Give the position of each P. falciparum parasite with its life-cycle stage, each leukocyte, and any debris.
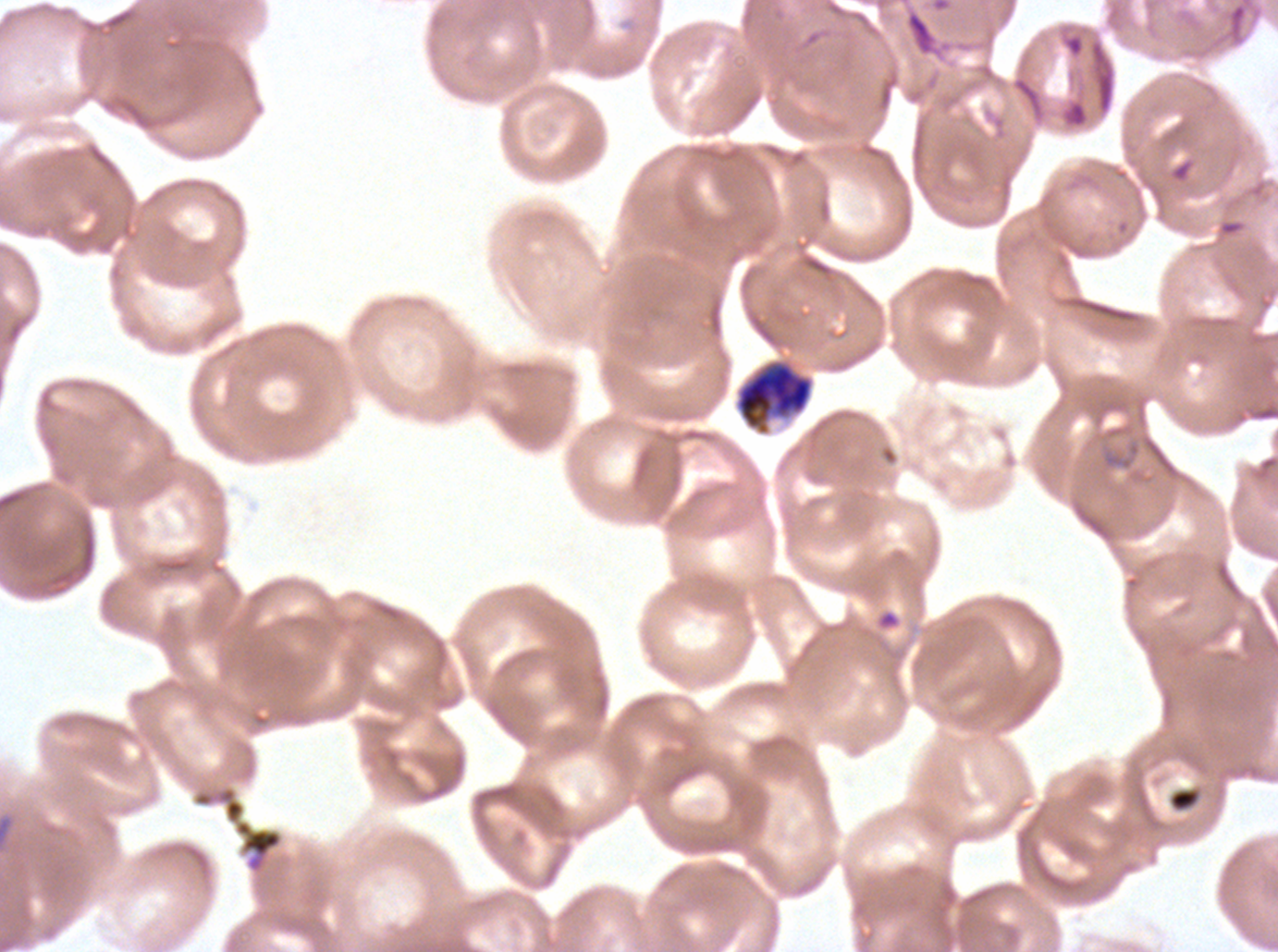

Approximate bounding boxes as (x1, y1, x2, y2) in pixels.
Late-ring/early-trophozoite forms: (1100, 438, 1142, 471).
Late trophozoites: (734, 359, 815, 436).
Debris: (191, 785, 284, 875).
No rings, mid trophozoites, early schizonts, late schizonts, segmenters, gametocytes, or leukocytes observed.

Summary:
  - Preparation: thin blood film
  - Specimen: P. falciparum cultured ex vivo for 24 to 48 hours, from a patient in The Gambia
  - Life-cycle stages observed: late-ring/early-trophozoite, late trophozoite
  - Image size: 1278×952 pixels
  - Field of view: sub-image separated from a larger composite
  - Stain: Giemsa